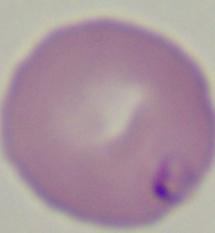

magnification = 1000x
modality = photomicrograph
identification = Babesia